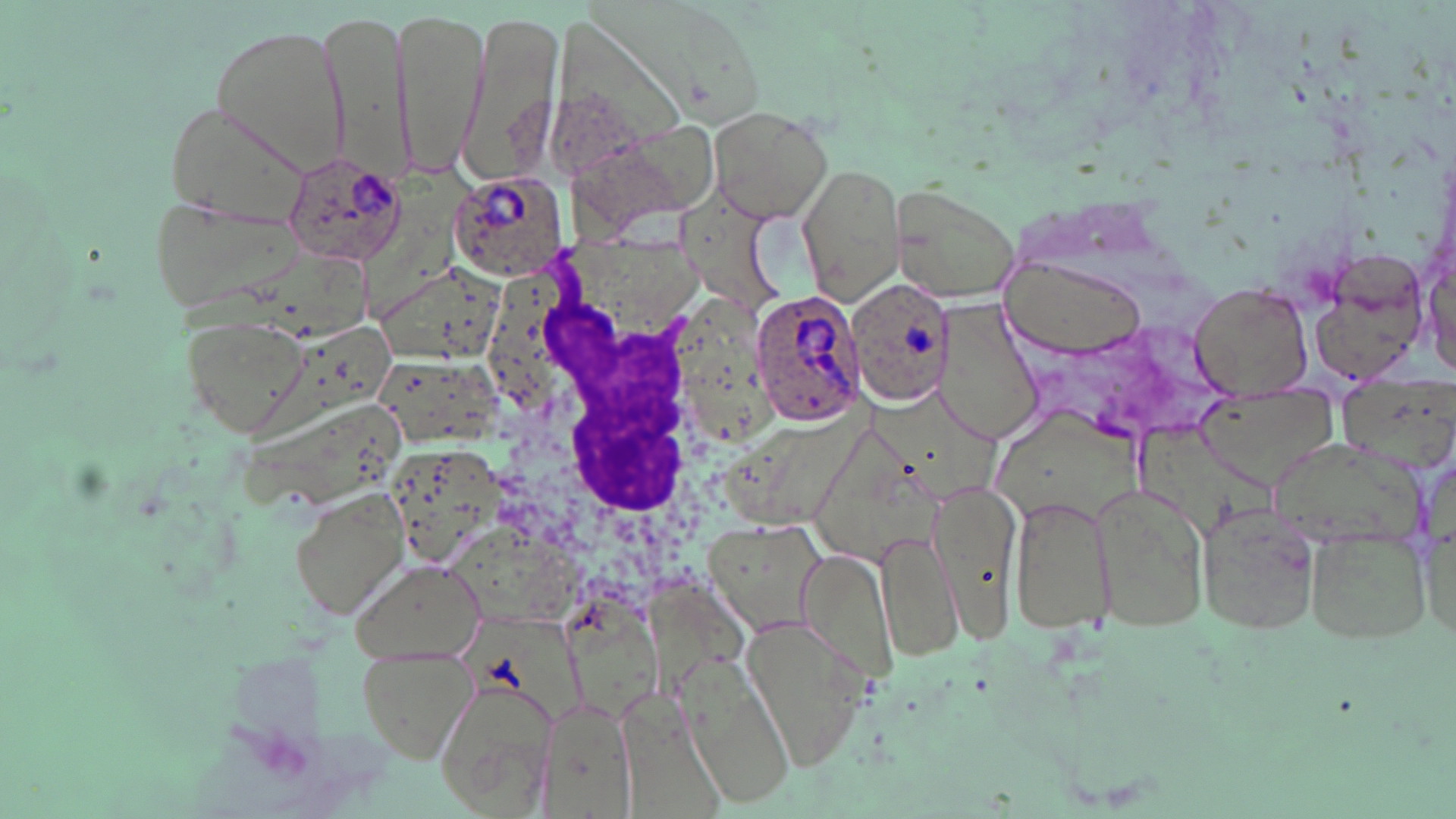
slide-level diagnosis = Plasmodium ovale
uninfected red blood cell locations = approximate bounding boxes as (x1, y1, x2, y2) in pixels: (397, 5, 485, 181), (320, 6, 409, 183), (460, 9, 565, 193), (209, 20, 351, 174), (162, 98, 309, 231), (706, 105, 835, 223), (799, 164, 906, 303), (889, 183, 1023, 307), (157, 193, 301, 314), (1301, 247, 1429, 383), (1000, 258, 1149, 359), (1189, 280, 1314, 399), (933, 300, 1043, 444), (180, 312, 315, 437), (1194, 385, 1335, 488), (1089, 476, 1211, 636), (929, 479, 1025, 640), (291, 489, 408, 620), (1008, 491, 1115, 634), (1200, 503, 1323, 639), (707, 518, 826, 636), (1304, 521, 1432, 646), (878, 527, 963, 662), (801, 548, 898, 679), (353, 557, 485, 660), (740, 615, 869, 767), (356, 638, 478, 764), (686, 664, 799, 811), (432, 678, 559, 818), (531, 694, 639, 819)
white blood cell locations = approximate bounding boxes as (x1, y1, x2, y2) in pixels: (492, 249, 757, 603)
magnification = 1000x
image size = 1456×819 pixels
modality = optical microscopy
preparation = thin blood film
Plasmodium ovale-infected red blood cell locations = approximate bounding boxes as (x1, y1, x2, y2) in pixels: (281, 152, 404, 269), (449, 169, 569, 281), (846, 279, 956, 410), (748, 288, 869, 430)
field of view = one of a larger specimen
stain = May-Grünwald-Giemsa